Identify the parasite.
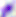

This is Toxoplasma gondii.

Summary:
  - Magnification: 400x
  - Modality: micrograph